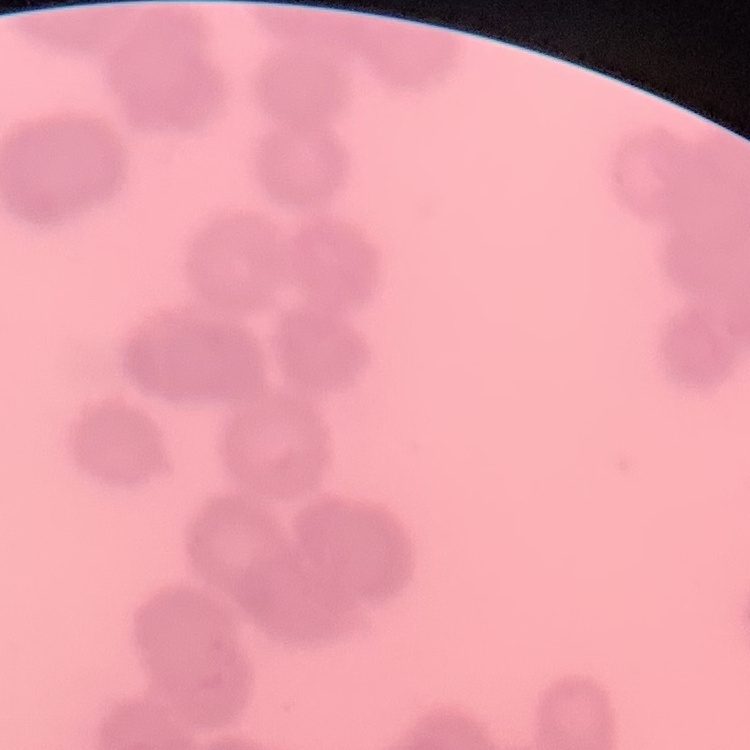
The erythrocytes show rouleaux formation. Field's or Giemsa stain. Thin peripheral smear. Square crop of a larger photomicrograph.